Name the blood parasite species.
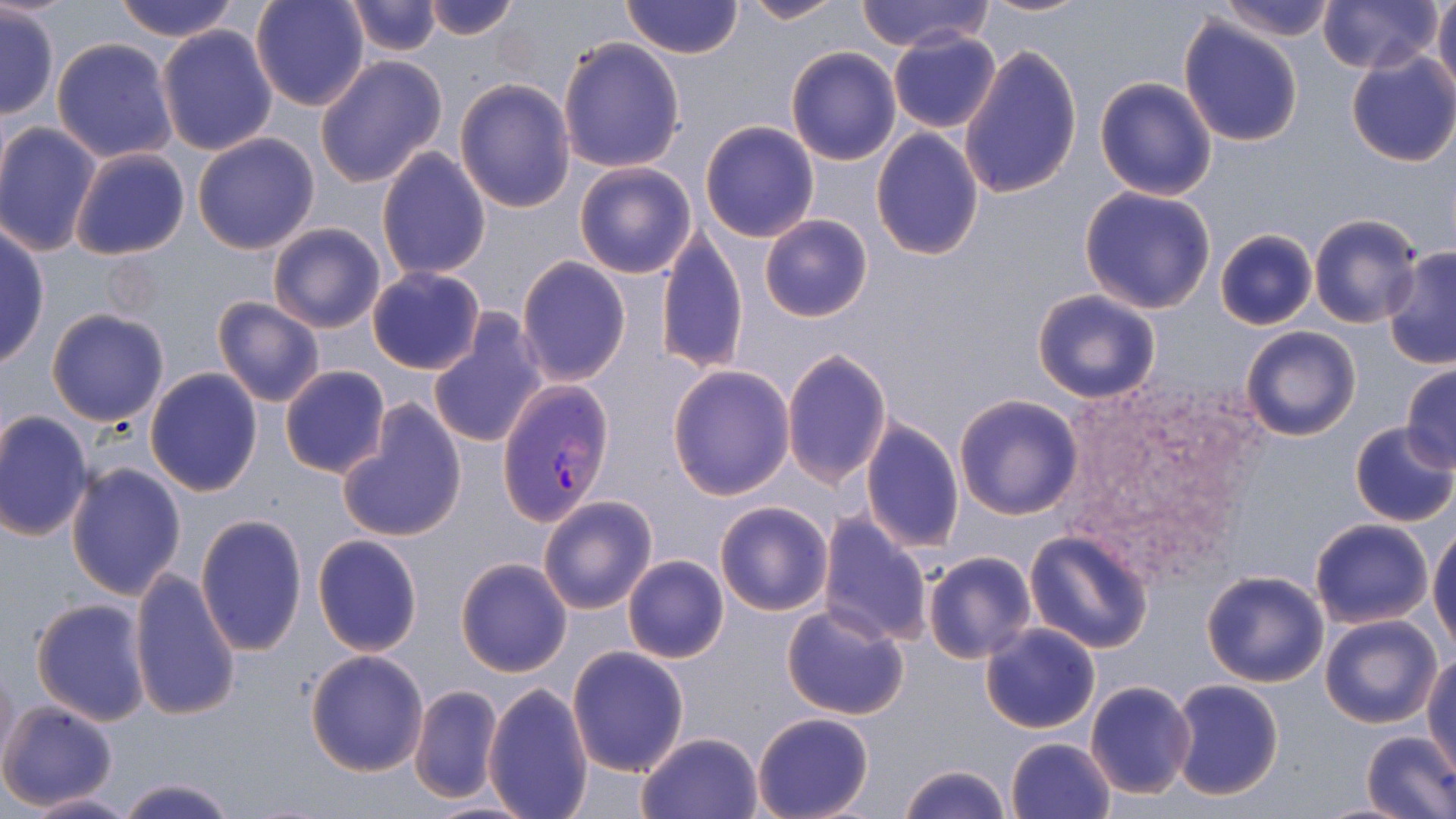
Plasmodium vivax.

Approximate bounding boxes as named x1/y1/x2/y2 corners in pixels. Plasmodium vivax-infected red blood cell locations: (x1=496, y1=382, x2=615, y2=524). Uninfected red blood cell locations: (x1=111, y1=0, x2=243, y2=43), (x1=250, y1=0, x2=372, y2=111), (x1=420, y1=0, x2=526, y2=41), (x1=621, y1=0, x2=744, y2=60), (x1=740, y1=0, x2=848, y2=24), (x1=975, y1=0, x2=1093, y2=18), (x1=1216, y1=0, x2=1338, y2=41), (x1=1317, y1=0, x2=1442, y2=73), (x1=1432, y1=0, x2=1456, y2=99), (x1=344, y1=1, x2=441, y2=57), (x1=856, y1=1, x2=990, y2=51), (x1=1, y1=6, x2=60, y2=119), (x1=1177, y1=16, x2=1304, y2=147), (x1=155, y1=25, x2=278, y2=156), (x1=888, y1=29, x2=1002, y2=133), (x1=51, y1=38, x2=179, y2=163), (x1=558, y1=38, x2=686, y2=173), (x1=958, y1=43, x2=1083, y2=200), (x1=786, y1=47, x2=900, y2=165), (x1=1345, y1=49, x2=1456, y2=167), (x1=315, y1=55, x2=448, y2=187), (x1=1094, y1=76, x2=1218, y2=200), (x1=455, y1=78, x2=577, y2=213), (x1=699, y1=120, x2=820, y2=242), (x1=0, y1=121, x2=102, y2=258), (x1=872, y1=128, x2=984, y2=260), (x1=191, y1=132, x2=320, y2=255), (x1=69, y1=146, x2=191, y2=261), (x1=376, y1=149, x2=492, y2=281), (x1=573, y1=161, x2=698, y2=279), (x1=1077, y1=186, x2=1218, y2=314), (x1=1308, y1=212, x2=1424, y2=329), (x1=760, y1=213, x2=872, y2=322), (x1=266, y1=222, x2=387, y2=334), (x1=0, y1=226, x2=50, y2=371), (x1=1213, y1=228, x2=1320, y2=331), (x1=656, y1=229, x2=747, y2=376), (x1=1382, y1=246, x2=1456, y2=370), (x1=516, y1=257, x2=632, y2=386), (x1=367, y1=266, x2=487, y2=375), (x1=1031, y1=288, x2=1162, y2=404), (x1=211, y1=296, x2=324, y2=406), (x1=45, y1=309, x2=171, y2=427), (x1=427, y1=313, x2=547, y2=449), (x1=1241, y1=326, x2=1361, y2=441), (x1=781, y1=348, x2=890, y2=488), (x1=666, y1=364, x2=795, y2=501), (x1=1400, y1=364, x2=1456, y2=468), (x1=279, y1=365, x2=391, y2=479), (x1=145, y1=368, x2=264, y2=496), (x1=953, y1=394, x2=1083, y2=518), (x1=337, y1=398, x2=468, y2=544), (x1=0, y1=410, x2=95, y2=541), (x1=861, y1=420, x2=964, y2=551), (x1=1349, y1=421, x2=1456, y2=527), (x1=65, y1=460, x2=189, y2=600), (x1=538, y1=495, x2=658, y2=613), (x1=715, y1=501, x2=834, y2=616), (x1=193, y1=512, x2=308, y2=656), (x1=817, y1=512, x2=934, y2=647), (x1=1309, y1=517, x2=1434, y2=628), (x1=1429, y1=524, x2=1456, y2=650), (x1=1024, y1=531, x2=1155, y2=656), (x1=311, y1=534, x2=423, y2=656), (x1=921, y1=550, x2=1037, y2=664), (x1=622, y1=555, x2=729, y2=664), (x1=456, y1=557, x2=572, y2=677), (x1=128, y1=567, x2=242, y2=723), (x1=1201, y1=570, x2=1330, y2=688), (x1=31, y1=598, x2=151, y2=726), (x1=781, y1=602, x2=911, y2=720), (x1=1318, y1=613, x2=1443, y2=729), (x1=980, y1=622, x2=1101, y2=734), (x1=567, y1=646, x2=688, y2=775), (x1=305, y1=648, x2=429, y2=775), (x1=1424, y1=657, x2=1456, y2=772), (x1=1, y1=663, x2=19, y2=777), (x1=1169, y1=679, x2=1284, y2=802), (x1=1084, y1=680, x2=1197, y2=800), (x1=483, y1=683, x2=594, y2=819), (x1=409, y1=685, x2=503, y2=803), (x1=0, y1=698, x2=120, y2=809), (x1=751, y1=713, x2=872, y2=819), (x1=637, y1=731, x2=764, y2=819), (x1=1360, y1=731, x2=1456, y2=819), (x1=1007, y1=736, x2=1116, y2=819), (x1=898, y1=764, x2=1011, y2=819), (x1=117, y1=776, x2=237, y2=818), (x1=18, y1=791, x2=145, y2=818). Thin blood film. May-Grünwald-Giemsa-stained preparation. Captured at 1000x magnification. One field of a larger specimen. Image is 1456×819 pixels. Light microscopy.